Assess the morphology of the red blood cells.
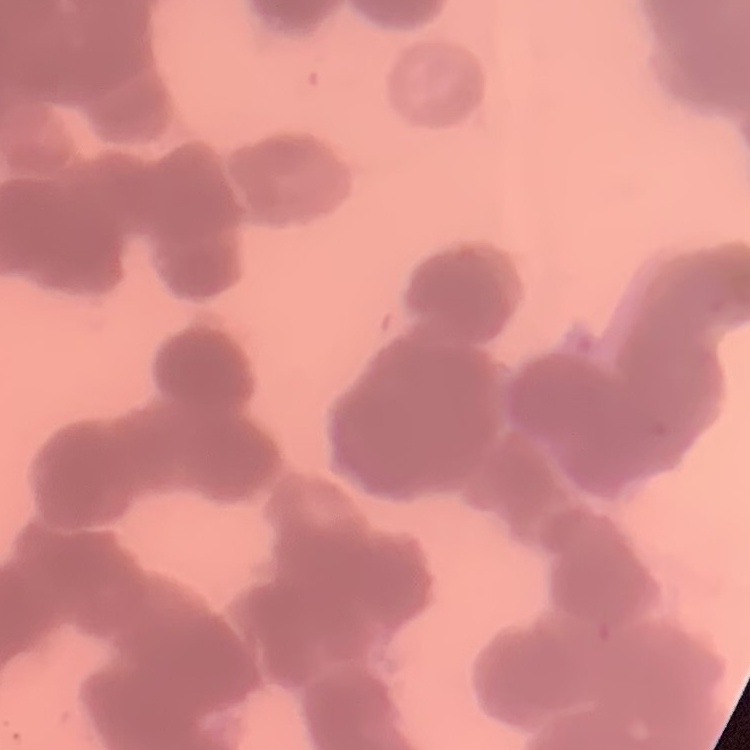
They show rouleaux formation.

stain: Field's or Giemsa
image_type: one tile cut from a larger photomicrograph
preparation: thin blood smear